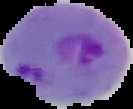

Summary:
  - Image type: segmented cell region with the area outside set to black
  - Preparation: thin blood film
  - Image size: 133×109 pixels
  - Result: Plasmodium parasites detected